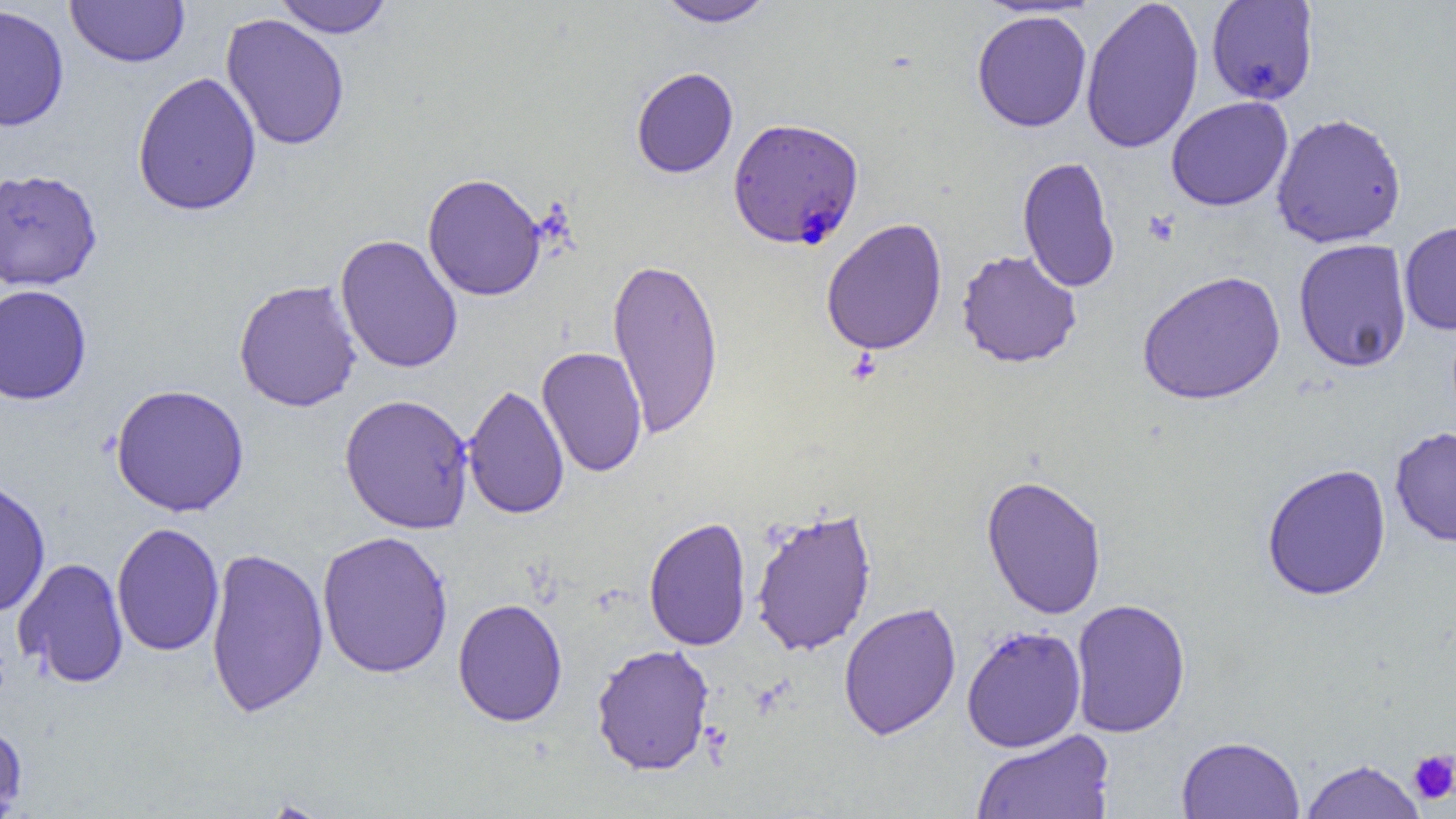
Approximate bounding boxes as named x1/y1/x2/y2 corners in pixels. Plasmodium falciparum-infected red blood cell locations: (x1=727, y1=118, x2=865, y2=252). Platelet locations: (x1=1142, y1=210, x2=1180, y2=247), (x1=1408, y1=749, x2=1456, y2=806). Uninfected red blood cell locations: (x1=65, y1=0, x2=189, y2=68), (x1=271, y1=0, x2=396, y2=38), (x1=654, y1=0, x2=776, y2=28), (x1=1080, y1=0, x2=1204, y2=155), (x1=1205, y1=0, x2=1319, y2=106), (x1=0, y1=4, x2=70, y2=132), (x1=971, y1=9, x2=1092, y2=133), (x1=220, y1=14, x2=350, y2=152), (x1=631, y1=68, x2=738, y2=179), (x1=132, y1=72, x2=262, y2=217), (x1=1166, y1=96, x2=1293, y2=212), (x1=1270, y1=112, x2=1407, y2=248), (x1=1016, y1=155, x2=1121, y2=294), (x1=0, y1=169, x2=103, y2=291), (x1=422, y1=173, x2=546, y2=302), (x1=821, y1=218, x2=948, y2=356), (x1=1398, y1=220, x2=1456, y2=336), (x1=335, y1=234, x2=463, y2=374), (x1=1293, y1=238, x2=1412, y2=373), (x1=956, y1=250, x2=1082, y2=369), (x1=606, y1=255, x2=725, y2=440), (x1=1137, y1=270, x2=1286, y2=406), (x1=233, y1=280, x2=362, y2=413), (x1=0, y1=284, x2=92, y2=405), (x1=536, y1=346, x2=648, y2=478), (x1=110, y1=384, x2=249, y2=517), (x1=463, y1=384, x2=570, y2=520), (x1=339, y1=394, x2=475, y2=535), (x1=1390, y1=427, x2=1456, y2=548), (x1=1260, y1=463, x2=1392, y2=601), (x1=980, y1=474, x2=1107, y2=620), (x1=0, y1=477, x2=52, y2=618), (x1=750, y1=506, x2=878, y2=657), (x1=643, y1=517, x2=752, y2=652), (x1=111, y1=522, x2=224, y2=657), (x1=316, y1=530, x2=454, y2=679), (x1=205, y1=547, x2=329, y2=719), (x1=14, y1=557, x2=129, y2=688), (x1=453, y1=598, x2=568, y2=727), (x1=1070, y1=599, x2=1191, y2=738), (x1=838, y1=602, x2=962, y2=741), (x1=961, y1=625, x2=1087, y2=752), (x1=591, y1=644, x2=715, y2=776), (x1=0, y1=720, x2=28, y2=818), (x1=971, y1=729, x2=1116, y2=819), (x1=1176, y1=735, x2=1305, y2=818), (x1=1299, y1=759, x2=1427, y2=819). Slide-level diagnosis: Plasmodium falciparum. Thin blood smear. Image is 1456×819 pixels. One field of a larger specimen. Optical microscopy. 1000x magnification.